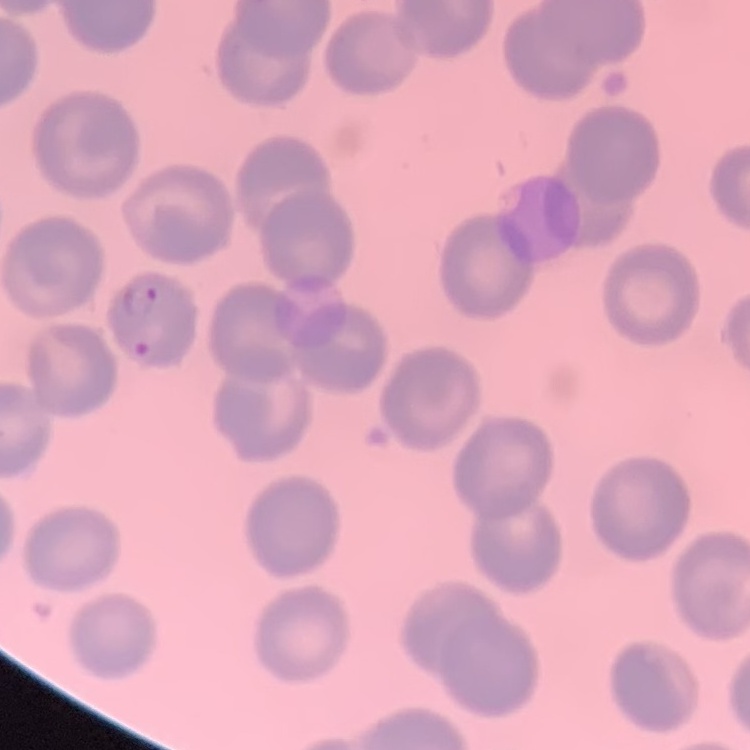

The red blood cells exhibit no rouleaux formation. One tile cut from a larger photomicrograph. Stained with either Field's or Giemsa. Thin blood smear.